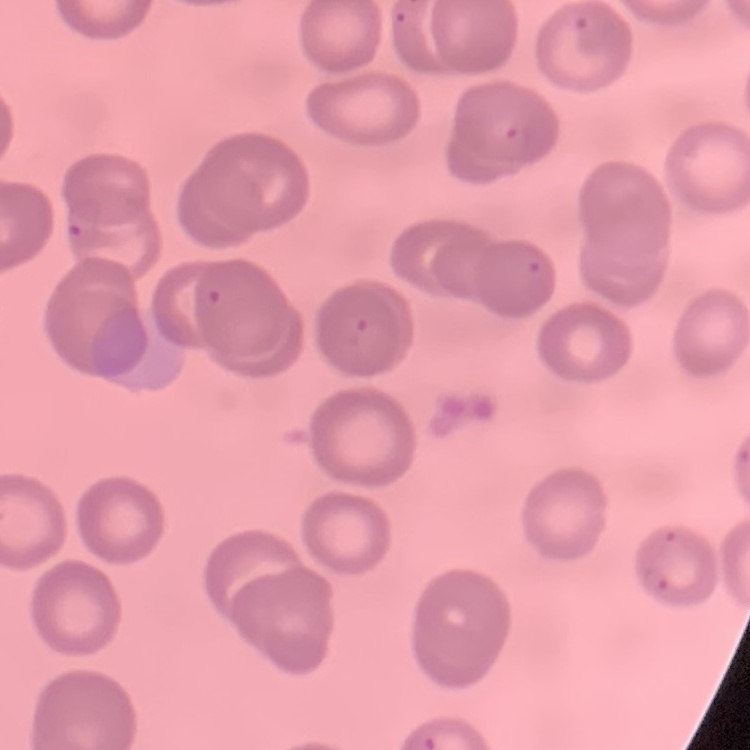 The erythrocytes show no rouleaux formation. Thin peripheral smear. Stained with either Field's or Giemsa. One tile cut from a larger photomicrograph.